Classify this cell by malaria status.
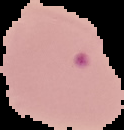
It is parasitized.

Summary:
  - Image size: 124×130 pixels
  - Image type: segmented cell region on a black background
  - Preparation: thin blood film